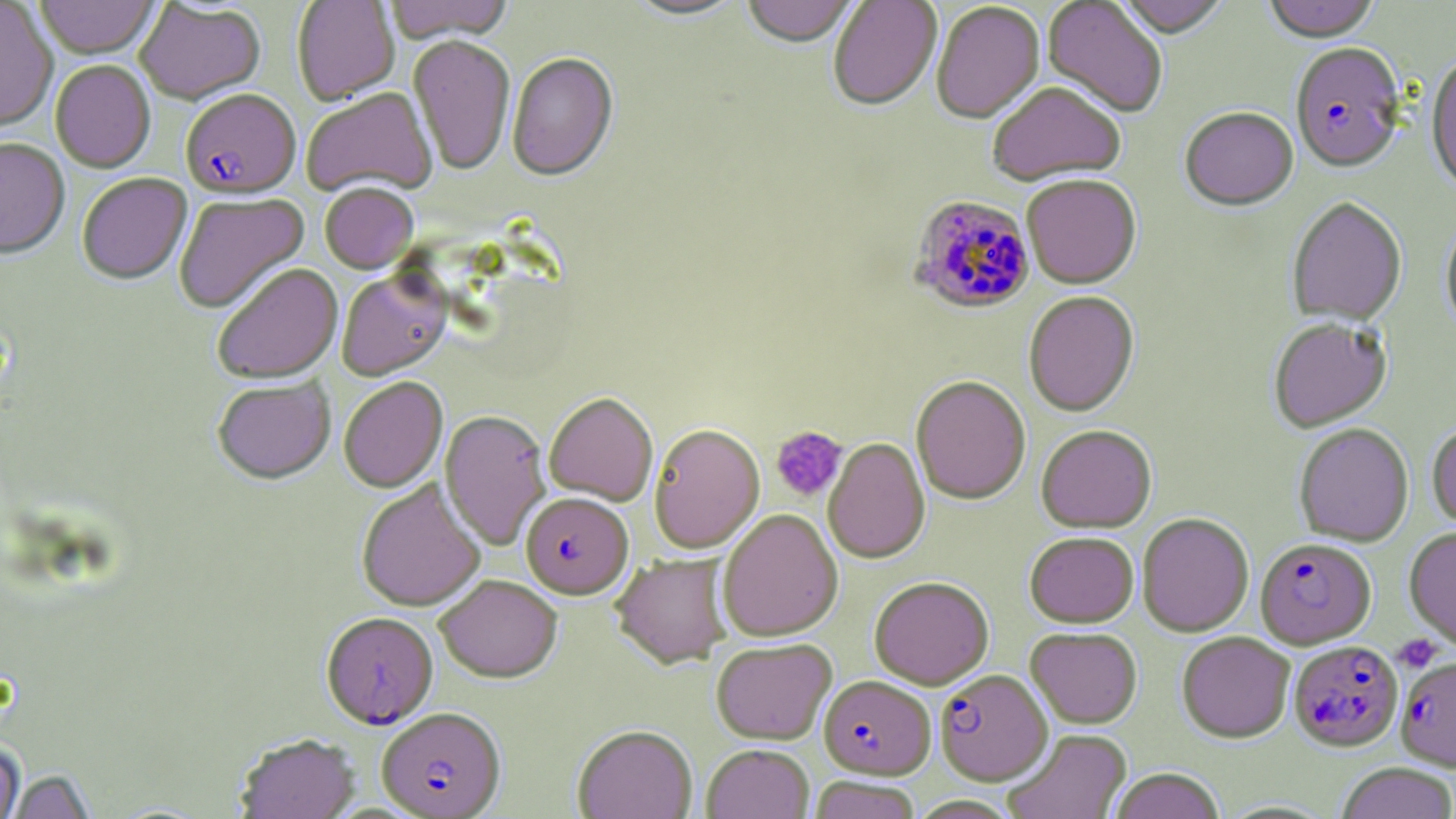 Approximate bounding boxes as (x1,y1)-(x2,y2) corner pairs in pixels. Platelet locations: (770,425)-(847,501), (1393,634)-(1443,673). Uninfected red blood cell locations: (35,0)-(159,60), (292,0)-(400,106), (384,0)-(514,44), (623,0)-(748,23), (741,0)-(858,50), (828,0)-(942,113), (1115,0)-(1231,39), (1262,0)-(1382,43), (1042,1)-(1169,119), (0,2)-(58,133), (135,2)-(265,106), (931,2)-(1045,126), (408,36)-(515,176), (1425,52)-(1456,197), (506,53)-(619,183), (50,60)-(155,174), (987,82)-(1126,187), (302,89)-(436,197), (1180,108)-(1298,212), (0,139)-(70,259), (77,173)-(192,285), (1022,175)-(1141,289), (320,183)-(419,274), (174,192)-(310,314), (1286,197)-(1407,326), (1440,215)-(1456,340), (212,264)-(343,384), (337,270)-(451,381), (1024,291)-(1139,417), (1267,317)-(1392,432), (339,376)-(448,493), (911,376)-(1030,505), (212,378)-(335,485), (543,393)-(658,506), (440,410)-(552,550), (1427,422)-(1456,529), (1294,423)-(1414,547), (648,424)-(765,554), (1036,424)-(1157,532), (823,438)-(930,564), (356,479)-(486,613), (717,509)-(843,642), (1137,513)-(1254,637), (1404,526)-(1456,651), (1025,531)-(1139,627), (611,554)-(732,670), (434,575)-(563,684), (869,576)-(994,689), (1025,626)-(1143,728), (1176,631)-(1294,743), (711,639)-(837,745), (572,726)-(697,819), (1003,729)-(1132,819), (235,734)-(360,818), (0,740)-(25,819), (702,745)-(814,819), (1336,762)-(1456,819), (1108,769)-(1226,819), (6,770)-(97,818), (808,776)-(922,819), (908,795)-(1022,819). Plasmodium falciparum-infected red blood cell locations: (1290,44)-(1406,175), (180,90)-(301,199), (909,194)-(1035,314), (521,492)-(633,599), (1255,538)-(1376,649), (320,613)-(436,729), (1289,640)-(1403,751), (1396,656)-(1456,769), (935,670)-(1052,785), (818,676)-(936,780), (377,707)-(506,818). Slide-level diagnosis: Plasmodium falciparum. Optical microscopy. Single field of view. Captured at 1000x magnification. May-Grünwald-Giemsa stain. Image is 1456×819 pixels. Thin blood smear.